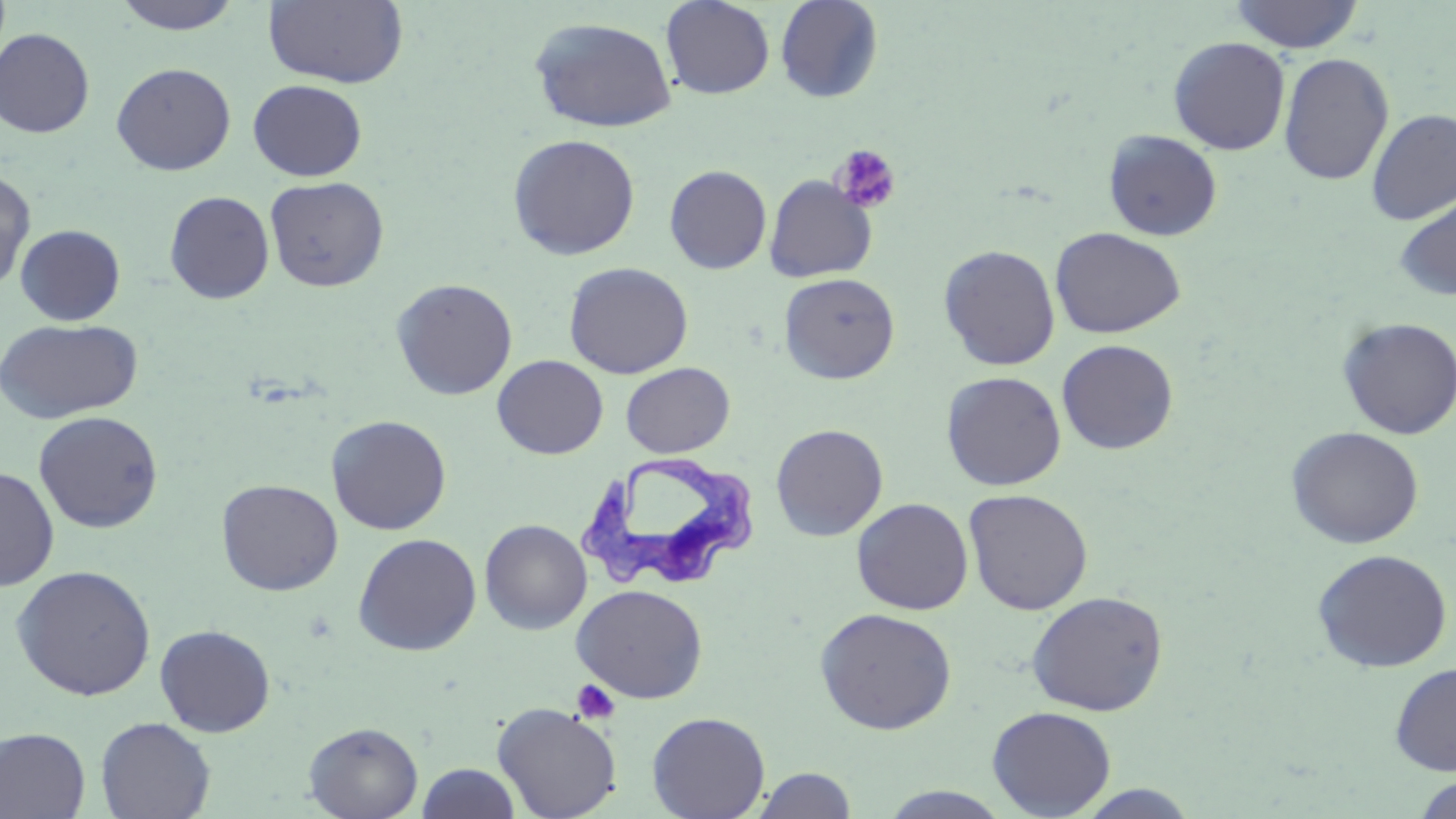
Approximate bounding boxes as (x1,y1)-(x2,y2) corner pairs in pixels. Uninfected red blood cell locations: (263,0)-(409,89), (660,0)-(775,99), (775,0)-(884,103), (1230,0)-(1364,53), (111,1)-(245,35), (528,16)-(678,134), (0,27)-(95,138), (1169,36)-(1290,155), (1278,52)-(1394,185), (111,62)-(236,175), (248,79)-(367,181), (1366,108)-(1456,224), (1103,129)-(1223,242), (507,133)-(641,260), (664,165)-(772,274), (0,166)-(37,291), (764,175)-(878,282), (264,176)-(390,292), (164,190)-(275,304), (1393,190)-(1456,303), (15,224)-(126,326), (1050,227)-(1186,339), (938,244)-(1061,371), (563,261)-(694,379), (779,272)-(900,384), (391,278)-(518,400), (1337,317)-(1456,439), (1,318)-(143,424), (1056,339)-(1178,454), (492,355)-(608,459), (621,362)-(735,457), (941,371)-(1066,491), (33,410)-(164,533), (326,414)-(451,535), (771,423)-(888,541), (1285,426)-(1424,549), (0,465)-(59,591), (216,478)-(343,596), (963,488)-(1093,615), (851,497)-(973,615), (479,518)-(593,635), (352,532)-(482,656), (1312,549)-(1453,672), (10,564)-(157,701), (571,583)-(708,703), (1026,590)-(1168,716), (814,607)-(958,735), (155,624)-(276,737), (1390,662)-(1456,775), (492,701)-(622,819), (987,706)-(1116,818), (647,711)-(770,819), (96,717)-(216,819), (303,722)-(423,819), (0,727)-(91,818), (416,763)-(523,819), (753,767)-(857,819), (1414,775)-(1455,818), (1074,784)-(1201,818), (876,786)-(1016,818). Platelet locations: (831,144)-(901,215), (571,679)-(620,724). Trypanosoma brucei locations: (578,451)-(760,595). Slide-level diagnosis: Trypanosoma brucei. Light microscopy. 1000x magnification. Thin blood smear. Single field of view. May-Grünwald-Giemsa-stained preparation. Image is 1456×819 pixels.